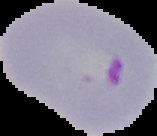

result: malaria parasites detected
image_size: 157×136 pixels
image_type: segmented cell region on a black background
preparation: thin blood film